Locate every uninfected red blood cell.
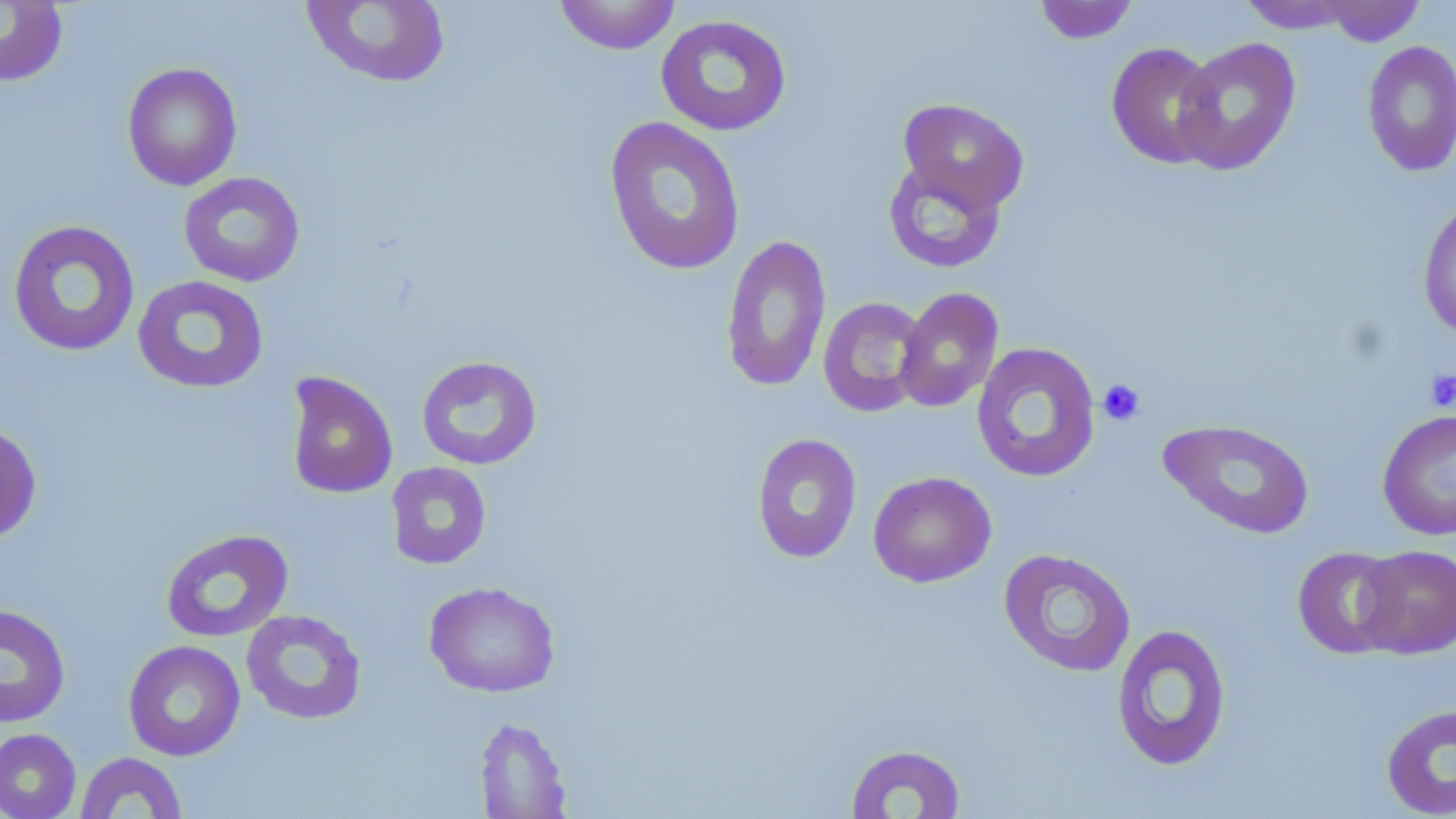
Approximate bounding boxes as [x1, y1, x2, y2] in pixels.
Uninfected red blood cells: [0, 0, 69, 87], [301, 0, 451, 89], [554, 0, 680, 55], [1032, 1, 1140, 44], [1238, 1, 1361, 33], [1315, 1, 1426, 46], [655, 14, 793, 136], [1172, 36, 1302, 176], [1361, 39, 1456, 177], [1105, 41, 1223, 169], [121, 62, 242, 191], [897, 97, 1029, 214], [603, 115, 746, 276], [883, 157, 1007, 273], [177, 171, 306, 287], [1417, 194, 1456, 341], [7, 219, 141, 357], [720, 233, 832, 393], [132, 275, 270, 394], [894, 286, 1004, 413], [818, 297, 929, 417], [971, 341, 1101, 483], [415, 355, 543, 470], [284, 371, 398, 499], [1377, 408, 1456, 541], [1158, 418, 1315, 539], [0, 422, 42, 544], [750, 432, 862, 564], [385, 461, 492, 570], [867, 470, 997, 588], [160, 529, 293, 643], [1356, 544, 1456, 658], [1292, 546, 1406, 659], [998, 547, 1137, 678], [423, 581, 560, 698], [0, 604, 70, 728], [240, 609, 367, 725], [1111, 622, 1232, 772], [123, 639, 246, 762], [1380, 703, 1456, 819], [474, 715, 572, 818], [0, 728, 81, 819], [844, 743, 966, 818], [74, 751, 188, 818].

Platelet locations: [1423, 368, 1456, 412], [1097, 378, 1145, 426]. Slide-level diagnosis: no evidence of blood parasites. May-Grünwald-Giemsa stain. Captured at 1000x magnification. Optical microscopy. One field of a larger specimen. Thin blood film. Image is 1456×819 pixels.